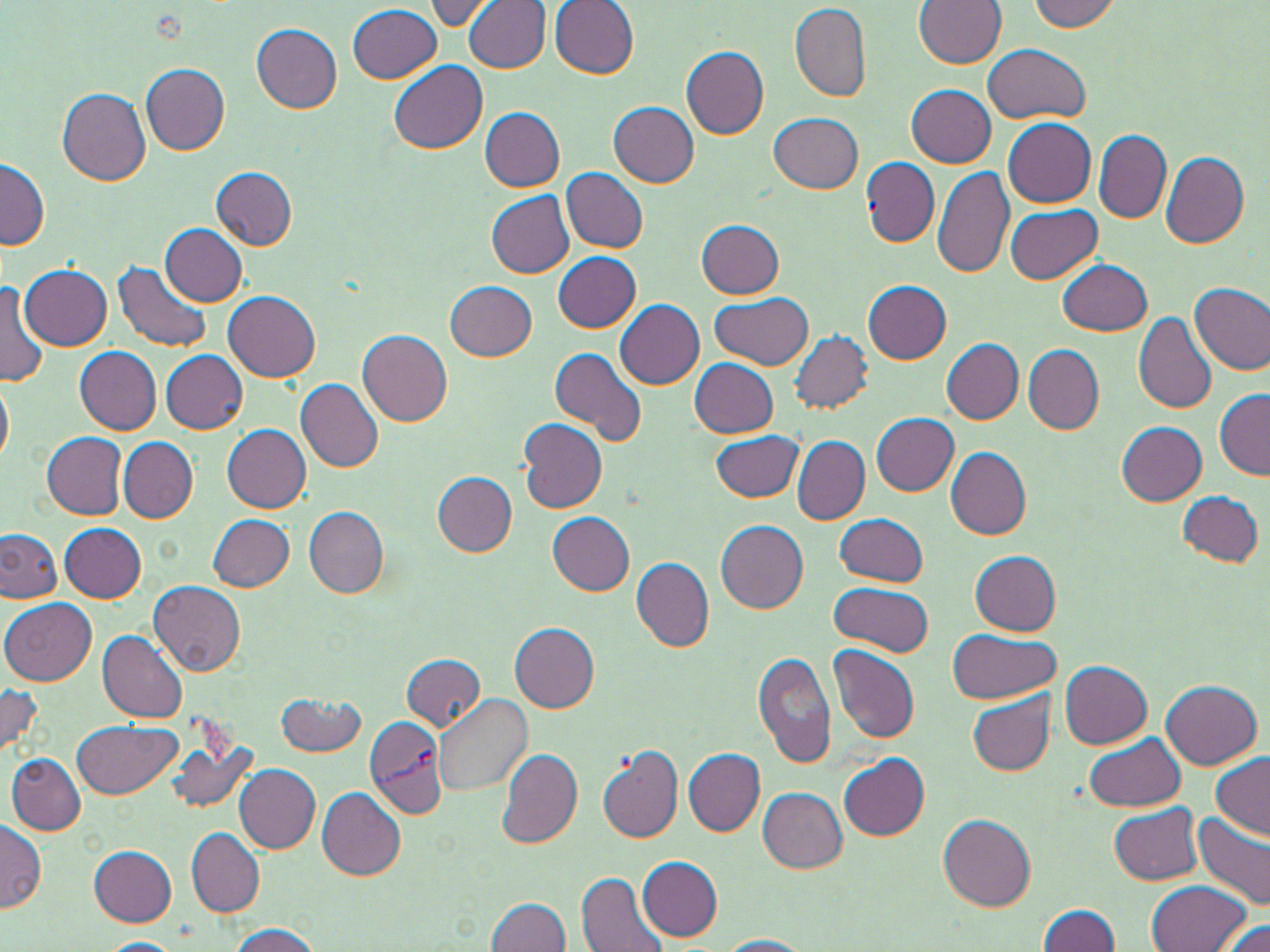

slide-level diagnosis = Plasmodium vivax
magnification = 1000x
Plasmodium vivax-infected red blood cell locations = approximate bounding boxes as named x1/y1/x2/y2 corners in pixels: (x1=364, y1=718, x2=448, y2=820)
uninfected red blood cell locations = approximate bounding boxes as named x1/y1/x2/y2 corners in pixels: (x1=419, y1=0, x2=505, y2=31), (x1=465, y1=0, x2=552, y2=72), (x1=914, y1=0, x2=1005, y2=68), (x1=1028, y1=0, x2=1121, y2=32), (x1=550, y1=1, x2=639, y2=78), (x1=347, y1=5, x2=441, y2=83), (x1=790, y1=5, x2=873, y2=102), (x1=251, y1=24, x2=341, y2=113), (x1=983, y1=44, x2=1092, y2=125), (x1=681, y1=46, x2=769, y2=139), (x1=389, y1=60, x2=487, y2=153), (x1=141, y1=62, x2=230, y2=154), (x1=907, y1=84, x2=996, y2=168), (x1=58, y1=87, x2=151, y2=186), (x1=609, y1=102, x2=699, y2=187), (x1=478, y1=107, x2=565, y2=191), (x1=769, y1=112, x2=863, y2=193), (x1=1003, y1=119, x2=1097, y2=208), (x1=1093, y1=130, x2=1171, y2=223), (x1=1159, y1=151, x2=1249, y2=248), (x1=0, y1=156, x2=50, y2=250), (x1=862, y1=156, x2=939, y2=246), (x1=211, y1=167, x2=297, y2=249), (x1=932, y1=167, x2=1014, y2=281), (x1=562, y1=168, x2=649, y2=253), (x1=485, y1=190, x2=574, y2=278), (x1=1005, y1=203, x2=1101, y2=284), (x1=695, y1=219, x2=784, y2=298), (x1=160, y1=224, x2=247, y2=306), (x1=553, y1=251, x2=641, y2=333), (x1=1057, y1=259, x2=1152, y2=335), (x1=114, y1=260, x2=210, y2=354), (x1=21, y1=265, x2=113, y2=351), (x1=0, y1=279, x2=51, y2=387), (x1=864, y1=280, x2=951, y2=363), (x1=445, y1=281, x2=536, y2=362), (x1=1191, y1=281, x2=1270, y2=374), (x1=224, y1=292, x2=320, y2=382), (x1=709, y1=292, x2=813, y2=370), (x1=615, y1=300, x2=705, y2=390), (x1=1133, y1=310, x2=1217, y2=414), (x1=357, y1=327, x2=452, y2=425), (x1=788, y1=330, x2=873, y2=415), (x1=942, y1=338, x2=1022, y2=423), (x1=1022, y1=344, x2=1104, y2=435), (x1=75, y1=346, x2=161, y2=433), (x1=549, y1=346, x2=648, y2=448), (x1=160, y1=350, x2=248, y2=433), (x1=690, y1=358, x2=780, y2=436), (x1=0, y1=375, x2=13, y2=466), (x1=295, y1=377, x2=383, y2=473), (x1=1214, y1=388, x2=1269, y2=479), (x1=872, y1=412, x2=959, y2=494), (x1=518, y1=418, x2=609, y2=514), (x1=1117, y1=422, x2=1207, y2=506), (x1=222, y1=424, x2=312, y2=512), (x1=710, y1=430, x2=803, y2=503), (x1=42, y1=433, x2=129, y2=517), (x1=118, y1=436, x2=197, y2=522), (x1=793, y1=436, x2=868, y2=525), (x1=945, y1=447, x2=1031, y2=539), (x1=430, y1=471, x2=518, y2=555), (x1=1177, y1=491, x2=1263, y2=567), (x1=303, y1=506, x2=388, y2=598), (x1=546, y1=512, x2=636, y2=594), (x1=209, y1=513, x2=294, y2=591), (x1=835, y1=513, x2=928, y2=586), (x1=715, y1=520, x2=809, y2=613), (x1=59, y1=521, x2=147, y2=602), (x1=0, y1=528, x2=62, y2=602), (x1=970, y1=550, x2=1061, y2=636), (x1=631, y1=558, x2=713, y2=653), (x1=149, y1=581, x2=244, y2=675), (x1=828, y1=583, x2=934, y2=658), (x1=2, y1=598, x2=98, y2=685), (x1=509, y1=624, x2=599, y2=712), (x1=947, y1=629, x2=1060, y2=704), (x1=98, y1=631, x2=189, y2=722), (x1=830, y1=646, x2=921, y2=742), (x1=755, y1=651, x2=839, y2=770), (x1=401, y1=654, x2=487, y2=731), (x1=1059, y1=662, x2=1151, y2=748), (x1=1161, y1=679, x2=1262, y2=769), (x1=0, y1=682, x2=45, y2=760), (x1=277, y1=692, x2=365, y2=756), (x1=435, y1=692, x2=533, y2=795), (x1=968, y1=693, x2=1055, y2=775), (x1=73, y1=720, x2=183, y2=799), (x1=1085, y1=732, x2=1186, y2=812), (x1=596, y1=741, x2=684, y2=843), (x1=169, y1=742, x2=259, y2=814), (x1=496, y1=746, x2=584, y2=851), (x1=684, y1=749, x2=764, y2=837), (x1=6, y1=752, x2=85, y2=834), (x1=838, y1=754, x2=929, y2=841), (x1=1210, y1=754, x2=1269, y2=841), (x1=233, y1=763, x2=319, y2=853), (x1=317, y1=787, x2=407, y2=880), (x1=758, y1=788, x2=847, y2=872), (x1=1108, y1=803, x2=1203, y2=885), (x1=1191, y1=813, x2=1270, y2=913), (x1=938, y1=815, x2=1036, y2=911), (x1=0, y1=820, x2=45, y2=913), (x1=186, y1=827, x2=265, y2=916), (x1=88, y1=844, x2=178, y2=926), (x1=636, y1=856, x2=723, y2=941), (x1=576, y1=873, x2=671, y2=952), (x1=1148, y1=881, x2=1250, y2=951), (x1=484, y1=896, x2=573, y2=952), (x1=1037, y1=905, x2=1120, y2=951), (x1=1216, y1=917, x2=1270, y2=952), (x1=223, y1=923, x2=324, y2=952), (x1=715, y1=935, x2=814, y2=952), (x1=99, y1=938, x2=183, y2=952)
preparation = thin blood smear
image size = 1270×952 pixels
field of view = one of a larger specimen
stain = May-Grünwald-Giemsa
modality = light microscopy